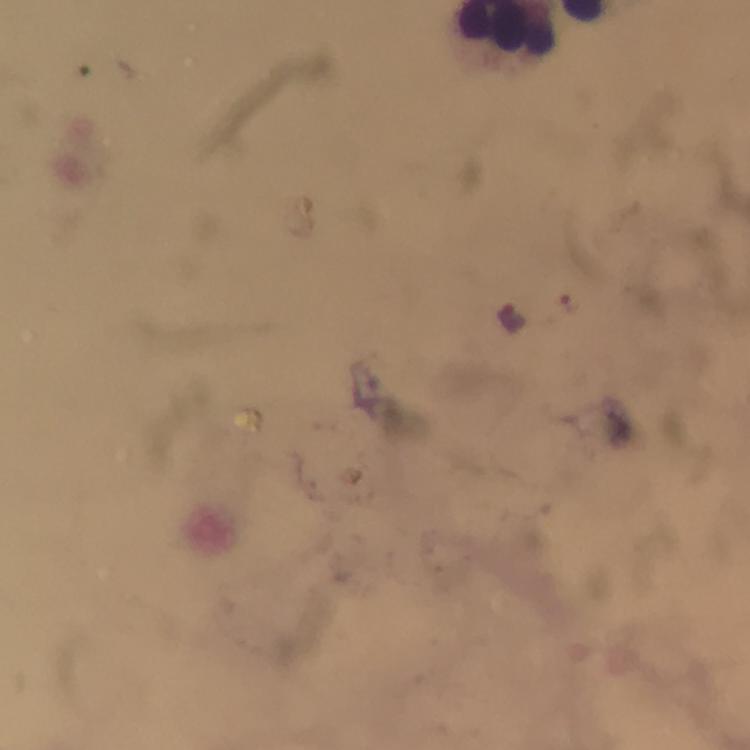

Approximate centers as {x, y} in pixels.
Summary:
  - Plasmodium parasite locations: {571, 305}, {512, 316}
  - Immersion oil: applied
  - Capture: smartphone mounted on the microscope
  - Stain: Giemsa
  - Cropped from: one field of view
  - Image size: 750×750 pixels
  - Magnification: 100x
  - Preparation: thick blood film
  - Context: from a diagnostic examination for malaria